Report the malaria status of this cell.
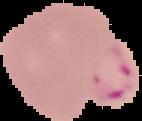

Parasitized.

Image is 142×121 pixels. From a thin blood film. Cell region segmented out of the field of view; the surrounding area is masked to black.